Comment on the morphology of the red blood cells.
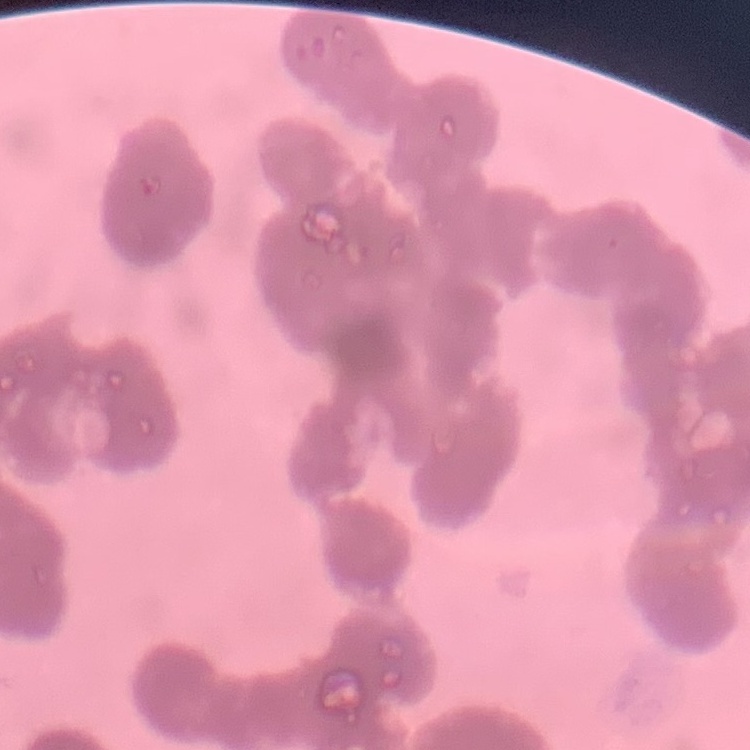
Rouleaux formation.

One tile cut from a larger photomicrograph. Thin blood film. Stained with either Field's or Giemsa.